Point out each Plasmodium parasite.
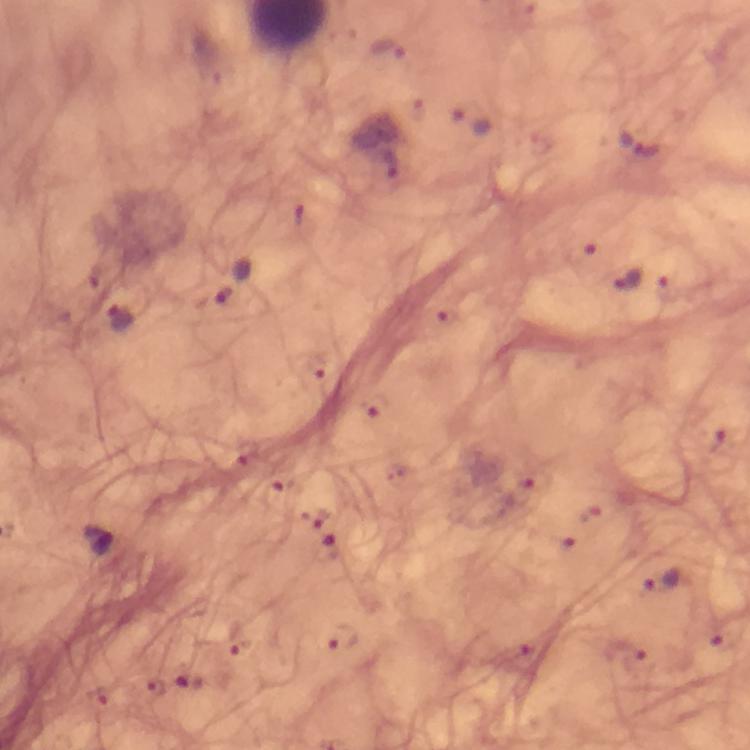
Approximate object centers, in pixels from the top-left corner.
Plasmodium parasites: (x=386, y=51), (x=470, y=121), (x=642, y=145), (x=387, y=163), (x=631, y=281), (x=233, y=282), (x=121, y=322), (x=318, y=364), (x=375, y=406), (x=244, y=459), (x=534, y=482), (x=316, y=517), (x=100, y=540), (x=327, y=549), (x=659, y=579), (x=341, y=637), (x=237, y=638), (x=188, y=680), (x=155, y=690), (x=100, y=700).

Summary:
  - Image size: 750×750 pixels
  - Cropped from: one field of view
  - Stain: Giemsa
  - Capture: smartphone photograph through a microscope
  - Context: from a malaria diagnostic workup
  - Immersion oil: used
  - Magnification: 100x
  - Preparation: thick blood smear